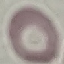
Summary:
  - Result: negative for malaria parasites
  - Capture: smartphone camera at the microscope eyepiece
  - Image type: cell patch, automatically extracted from a larger field of view and resized to 64 × 64 pixels
  - Preparation: thin blood smear
  - Stain: Giemsa